Assess this cell for malaria.
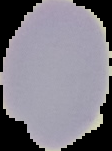
Parasitized.

preparation = thin blood smear
image size = 112×151 pixels
image type = segmented cell region with the area outside set to black